Identify the parasite.
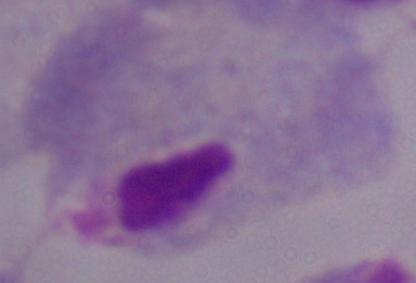

A trichomonad.

Photomicrograph. Captured at 1000x magnification.